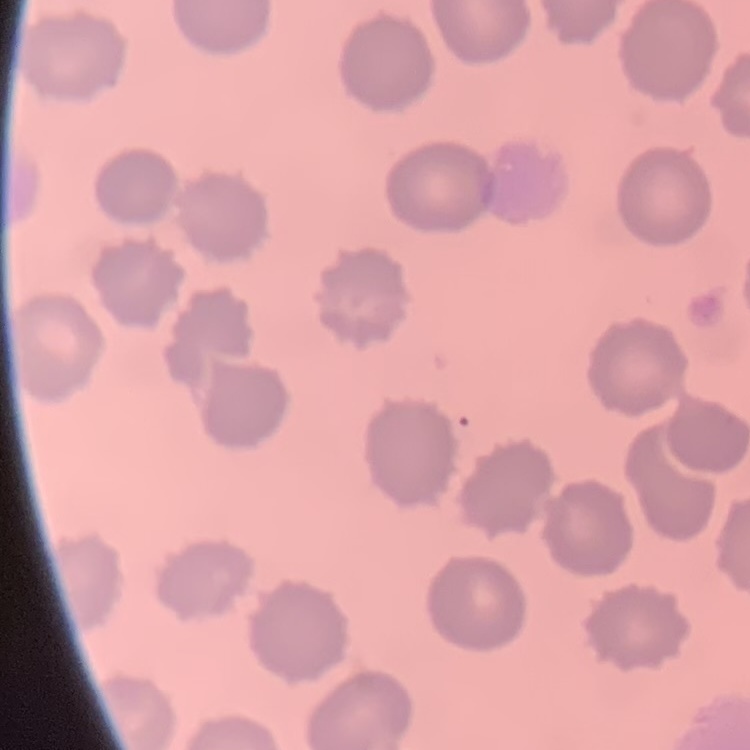

red blood cell morphology = no rouleaux formation
image type = one tile cut from a larger photomicrograph
preparation = thin peripheral smear
stain = Field's or Giemsa